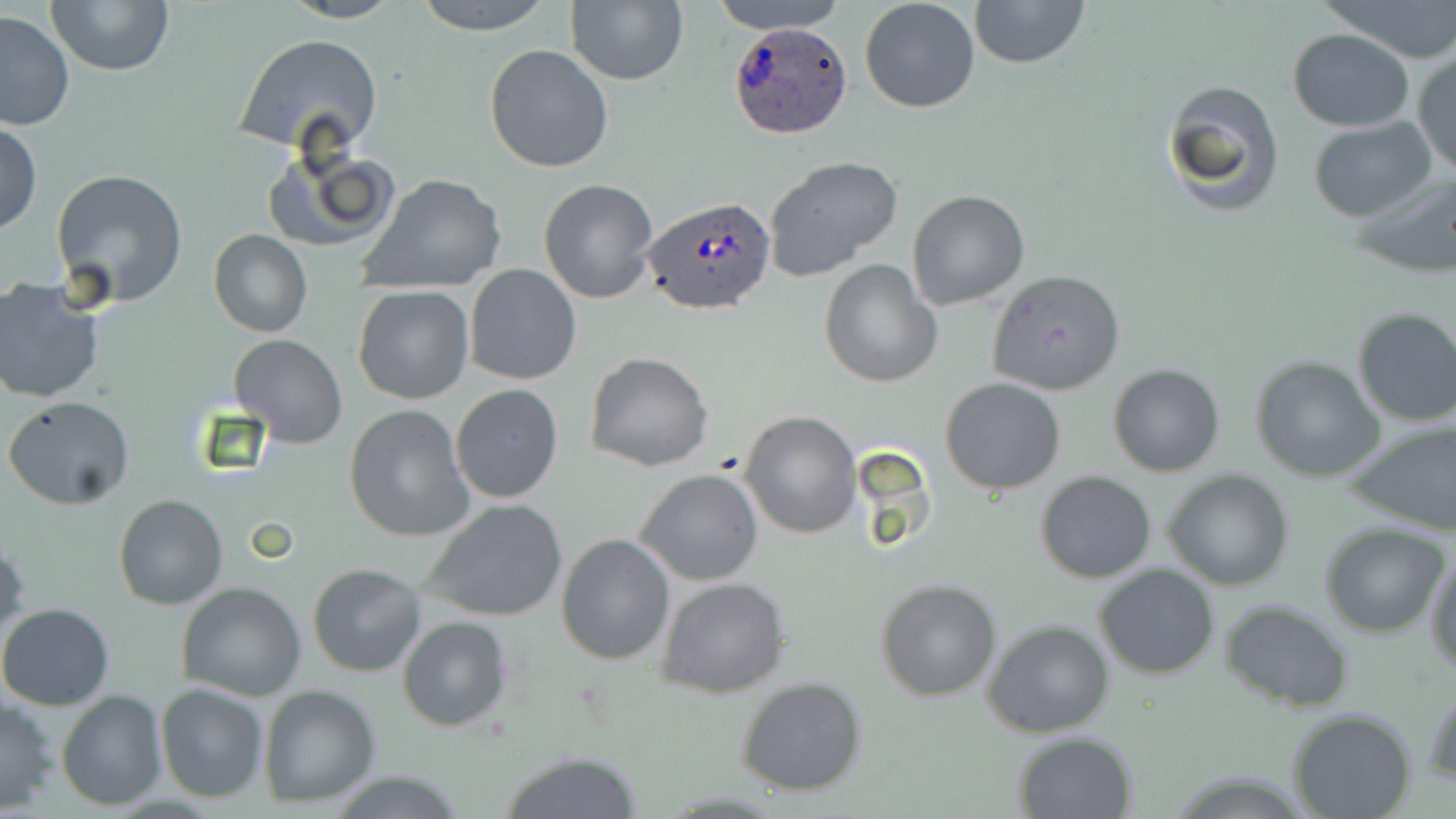

Plasmodium ovale-infected red blood cell locations = approximate bounding boxes as named x1/y1/x2/y2 corners in pixels: (x1=728, y1=19, x2=854, y2=138), (x1=642, y1=195, x2=777, y2=317)
slide-level diagnosis = Plasmodium ovale
field of view = one of a larger specimen
uninfected red blood cell locations = approximate bounding boxes as named x1/y1/x2/y2 corners in pixels: (x1=47, y1=0, x2=175, y2=75), (x1=278, y1=0, x2=406, y2=24), (x1=412, y1=0, x2=553, y2=36), (x1=707, y1=0, x2=850, y2=34), (x1=859, y1=0, x2=981, y2=114), (x1=967, y1=0, x2=1091, y2=71), (x1=1320, y1=0, x2=1456, y2=64), (x1=565, y1=1, x2=688, y2=85), (x1=0, y1=9, x2=76, y2=131), (x1=1287, y1=29, x2=1416, y2=131), (x1=233, y1=32, x2=383, y2=159), (x1=485, y1=44, x2=615, y2=174), (x1=1411, y1=47, x2=1456, y2=178), (x1=1160, y1=79, x2=1285, y2=218), (x1=1309, y1=117, x2=1437, y2=220), (x1=0, y1=121, x2=43, y2=234), (x1=262, y1=142, x2=399, y2=256), (x1=763, y1=156, x2=906, y2=285), (x1=52, y1=168, x2=187, y2=307), (x1=1351, y1=170, x2=1456, y2=278), (x1=359, y1=173, x2=508, y2=295), (x1=537, y1=177, x2=661, y2=304), (x1=907, y1=190, x2=1031, y2=312), (x1=208, y1=231, x2=311, y2=338), (x1=821, y1=260, x2=940, y2=388), (x1=465, y1=264, x2=581, y2=385), (x1=986, y1=269, x2=1125, y2=395), (x1=0, y1=277, x2=105, y2=403), (x1=353, y1=284, x2=474, y2=404), (x1=1350, y1=307, x2=1456, y2=428), (x1=229, y1=334, x2=348, y2=448), (x1=585, y1=352, x2=713, y2=473), (x1=1250, y1=354, x2=1388, y2=482), (x1=1107, y1=364, x2=1224, y2=477), (x1=940, y1=377, x2=1067, y2=496), (x1=449, y1=383, x2=563, y2=503), (x1=4, y1=396, x2=135, y2=511), (x1=344, y1=404, x2=475, y2=542), (x1=739, y1=410, x2=863, y2=539), (x1=1345, y1=417, x2=1456, y2=535), (x1=635, y1=468, x2=765, y2=586), (x1=643, y1=470, x2=776, y2=696), (x1=1162, y1=470, x2=1295, y2=591), (x1=1035, y1=471, x2=1157, y2=584), (x1=113, y1=493, x2=228, y2=610), (x1=423, y1=498, x2=569, y2=623), (x1=1320, y1=523, x2=1451, y2=639), (x1=556, y1=532, x2=674, y2=666), (x1=0, y1=535, x2=28, y2=645), (x1=1426, y1=552, x2=1456, y2=675), (x1=308, y1=563, x2=426, y2=679), (x1=1093, y1=564, x2=1220, y2=679), (x1=657, y1=576, x2=791, y2=699), (x1=875, y1=578, x2=1004, y2=702), (x1=176, y1=582, x2=307, y2=702), (x1=1218, y1=600, x2=1355, y2=712), (x1=0, y1=603, x2=116, y2=711), (x1=398, y1=615, x2=514, y2=731), (x1=983, y1=619, x2=1115, y2=736), (x1=735, y1=675, x2=869, y2=797), (x1=155, y1=682, x2=268, y2=803), (x1=1424, y1=684, x2=1456, y2=788), (x1=258, y1=685, x2=381, y2=807), (x1=57, y1=691, x2=168, y2=810), (x1=0, y1=696, x2=60, y2=814), (x1=1287, y1=709, x2=1418, y2=819), (x1=1012, y1=731, x2=1137, y2=817), (x1=498, y1=749, x2=642, y2=818)
magnification = 1000x
preparation = thin blood film
image size = 1456×819 pixels
stain = May-Grünwald-Giemsa
modality = light microscopy